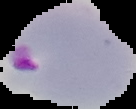
The area outside the segmented cell region is set to black. From a thin blood smear. Image is 136×109 pixels. Result: malaria parasites detected.